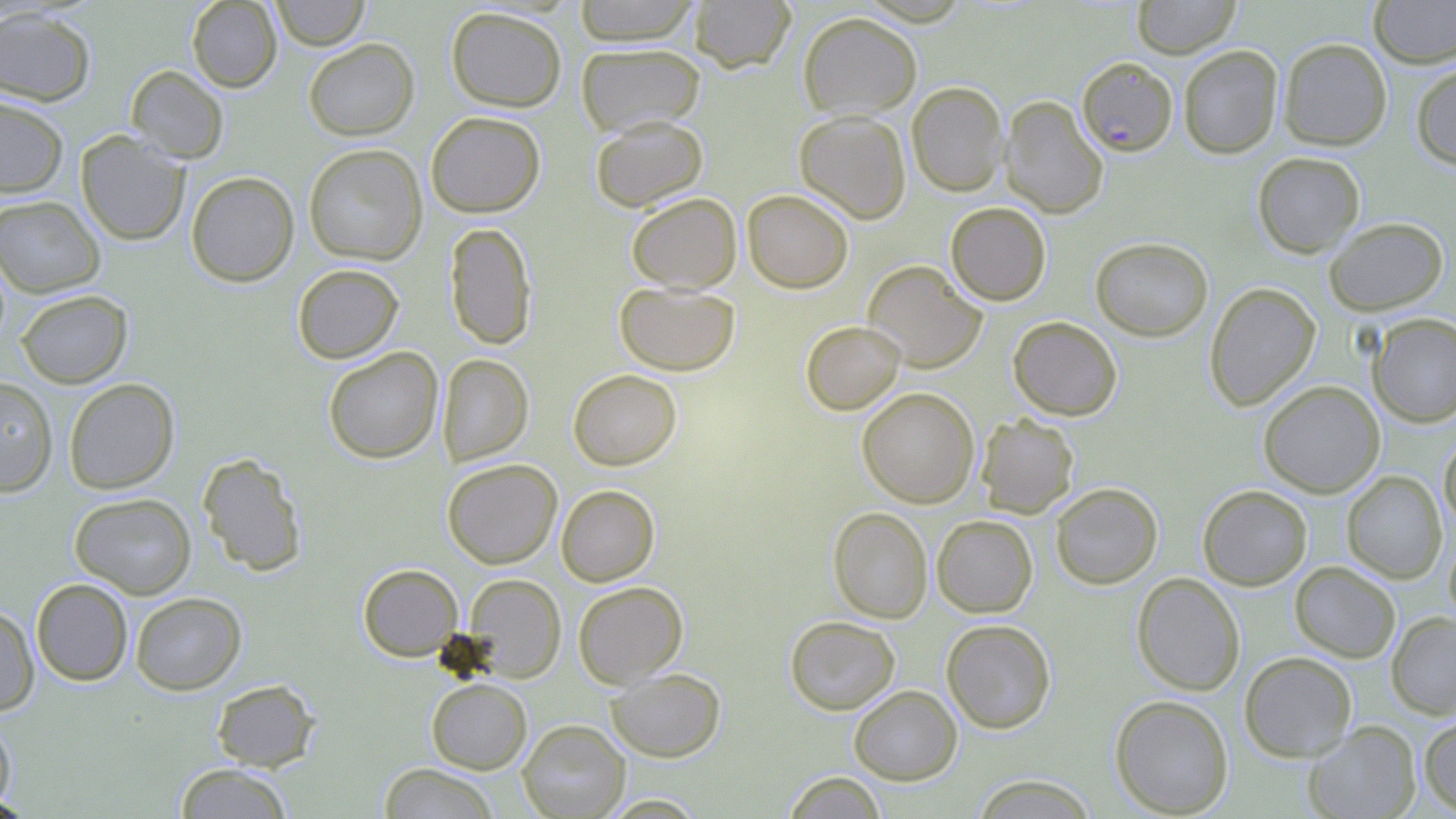

slide-level diagnosis = Plasmodium falciparum
modality = optical microscopy
Plasmodium falciparum-infected red blood cell locations = approximate bounding boxes as (x1,y1)-(x2,y2) corner pairs in pixels: (1077,56)-(1177,156)
magnification = 1000x
uninfected red blood cell locations = approximate bounding boxes as (x1,y1)-(x2,y2) corner pairs in pixels: (187,0)-(282,92), (269,0)-(370,51), (572,0)-(701,46), (688,0)-(796,73), (1132,0)-(1240,58), (1369,0)-(1456,67), (0,6)-(97,106), (446,6)-(567,112), (797,12)-(923,119), (303,38)-(419,140), (1278,38)-(1392,151), (576,42)-(705,136), (1178,45)-(1283,159), (1411,61)-(1456,170), (126,65)-(229,163), (907,81)-(1008,197), (0,95)-(69,198), (1000,95)-(1108,218), (794,110)-(912,224), (425,111)-(545,217), (590,115)-(708,211), (75,130)-(190,246), (303,144)-(428,265), (1252,151)-(1365,257), (186,171)-(300,287), (742,189)-(854,293), (626,192)-(742,292), (0,195)-(106,298), (945,202)-(1051,305), (1324,217)-(1449,315), (444,222)-(538,350), (1090,236)-(1214,341), (862,260)-(987,372), (291,263)-(404,364), (615,282)-(740,376), (1204,282)-(1321,411), (16,289)-(132,388), (1368,313)-(1456,428), (1008,316)-(1123,420), (800,320)-(905,415), (323,347)-(443,464), (437,353)-(533,466), (568,369)-(682,470), (0,376)-(58,497), (64,378)-(180,493), (1258,380)-(1385,498), (856,387)-(980,508), (976,414)-(1079,518), (1439,433)-(1456,533), (198,453)-(308,576), (442,459)-(562,569), (1342,471)-(1447,583), (1050,482)-(1163,589), (556,484)-(660,586), (1197,485)-(1312,590), (69,492)-(197,599), (828,506)-(933,623), (931,514)-(1038,618), (1444,535)-(1456,631), (1290,562)-(1401,662), (358,563)-(463,661), (1132,572)-(1245,696), (464,573)-(566,682), (31,578)-(133,686), (573,581)-(688,687), (130,592)-(246,695), (0,605)-(40,716), (1387,612)-(1456,719), (784,616)-(900,714), (941,619)-(1056,733), (1239,651)-(1357,762), (606,668)-(726,762), (427,678)-(532,774), (211,679)-(319,771), (848,685)-(962,785), (1109,694)-(1234,817), (0,714)-(17,813), (1419,714)-(1456,815), (517,719)-(630,818), (1303,721)-(1421,818), (173,763)-(293,818), (379,763)-(500,818), (781,771)-(887,818), (969,774)-(1099,818), (0,794)-(36,818), (597,794)-(709,817)
stain = May-Grünwald-Giemsa
preparation = thin blood smear
image size = 1456×819 pixels
field of view = one of a larger specimen